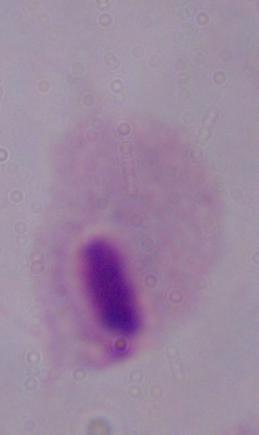 A trichomonad is seen. Captured at 1000x magnification. Micrograph.